Identify the parasite.
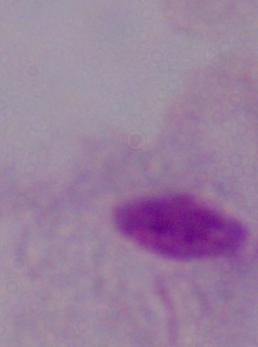
A trichomonad.

modality = photomicrograph
magnification = 1000x